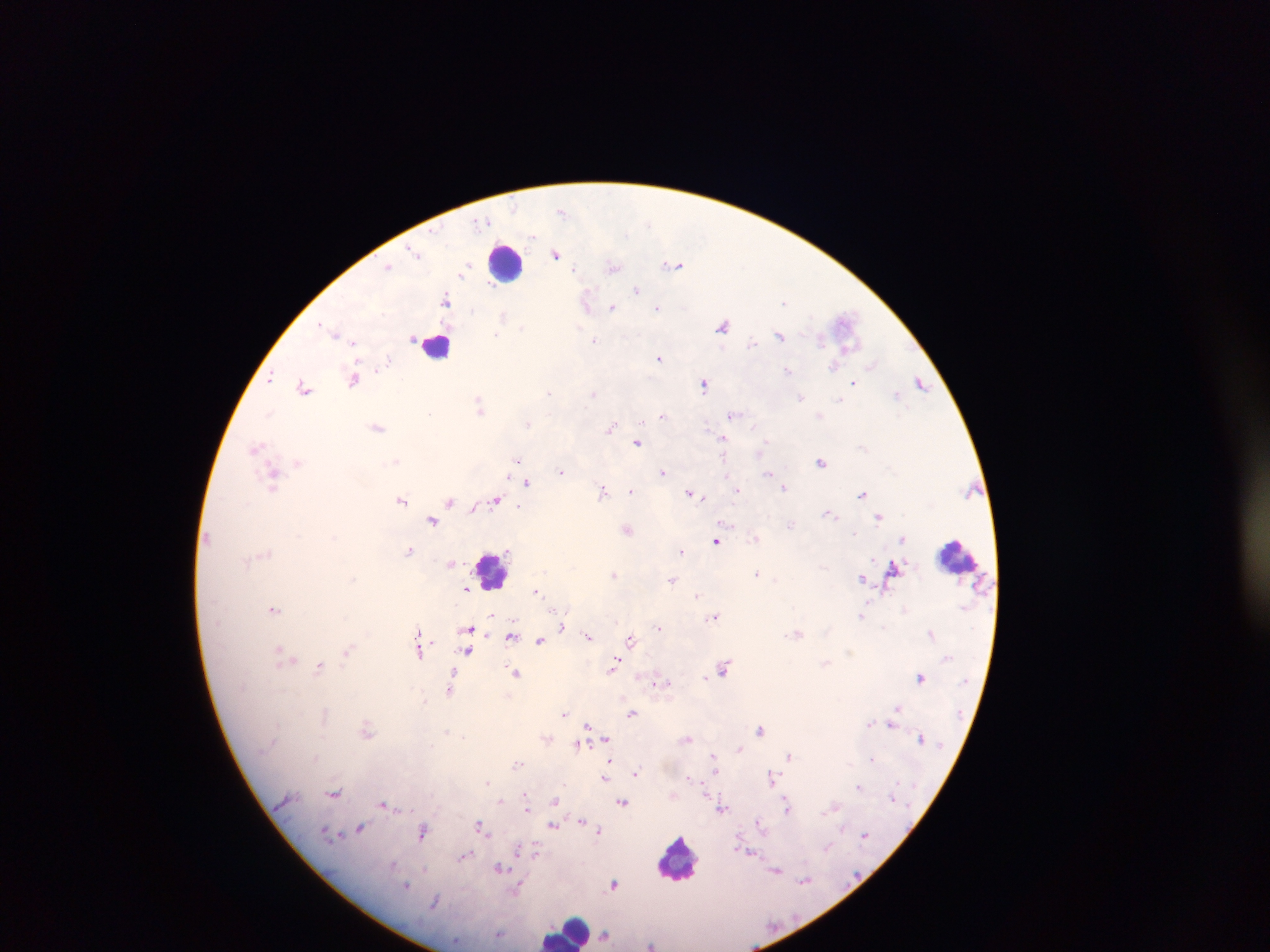

Approximate centers as [x, y] in pixels.
Summary:
  - Malaria parasite locations: [563, 210], [416, 253], [556, 254], [677, 265], [614, 266], [388, 267], [637, 289], [446, 299], [586, 301], [613, 307], [657, 307], [504, 314], [845, 321], [725, 325], [334, 332], [780, 336], [594, 339], [660, 357], [872, 365], [788, 370], [270, 377], [355, 377], [920, 382], [854, 383], [704, 384], [304, 387], [550, 392], [593, 392], [897, 394], [480, 405], [734, 413], [663, 415], [528, 422], [378, 427], [611, 427], [723, 438], [638, 442], [255, 447], [517, 458], [822, 461], [299, 462], [561, 471], [663, 472], [768, 473], [274, 475], [527, 481], [784, 487], [738, 489], [631, 490], [605, 491], [690, 492], [862, 493], [699, 496], [497, 499], [402, 500], [451, 500], [474, 507], [831, 514], [879, 516], [433, 520], [628, 529], [903, 538], [717, 540], [410, 550], [682, 551], [450, 562], [894, 568], [615, 574], [757, 574], [863, 577], [672, 579], [466, 589], [537, 591], [274, 608], [863, 614], [493, 615], [716, 615], [562, 626], [660, 628], [470, 629], [419, 631], [798, 632], [931, 633], [589, 635], [511, 636], [540, 639], [632, 639], [420, 640], [280, 649], [420, 650], [468, 650], [348, 651], [287, 659], [321, 665], [614, 666], [724, 667], [454, 672], [517, 673], [921, 676], [659, 682], [451, 688], [423, 700], [897, 709], [564, 713], [633, 713], [869, 724], [893, 725], [588, 726], [761, 729], [367, 730], [448, 733], [688, 738], [547, 739], [606, 740], [579, 743], [740, 748], [789, 755], [713, 756], [518, 762], [609, 764], [636, 772], [606, 777], [773, 778], [487, 781], [860, 787], [335, 793], [527, 794], [556, 800], [501, 801], [623, 801], [384, 804], [786, 805], [835, 806], [528, 808], [722, 808], [581, 820], [760, 823], [554, 825], [481, 826], [361, 827], [600, 830], [424, 831], [864, 836], [828, 846], [519, 850], [536, 851], [500, 868], [777, 870], [805, 880], [614, 884], [407, 885], [519, 888], [500, 934], [605, 935], [652, 944]
  - Leukocyte locations: [505, 261], [436, 345], [959, 556], [492, 571], [679, 859], [567, 932]
  - Capture: mobile-phone photograph through a microscope
  - Image size: 1270×952 pixels
  - Field of view: single
  - Preparation: thick blood film
  - Country: Ghana